Locate every parasitized RBC.
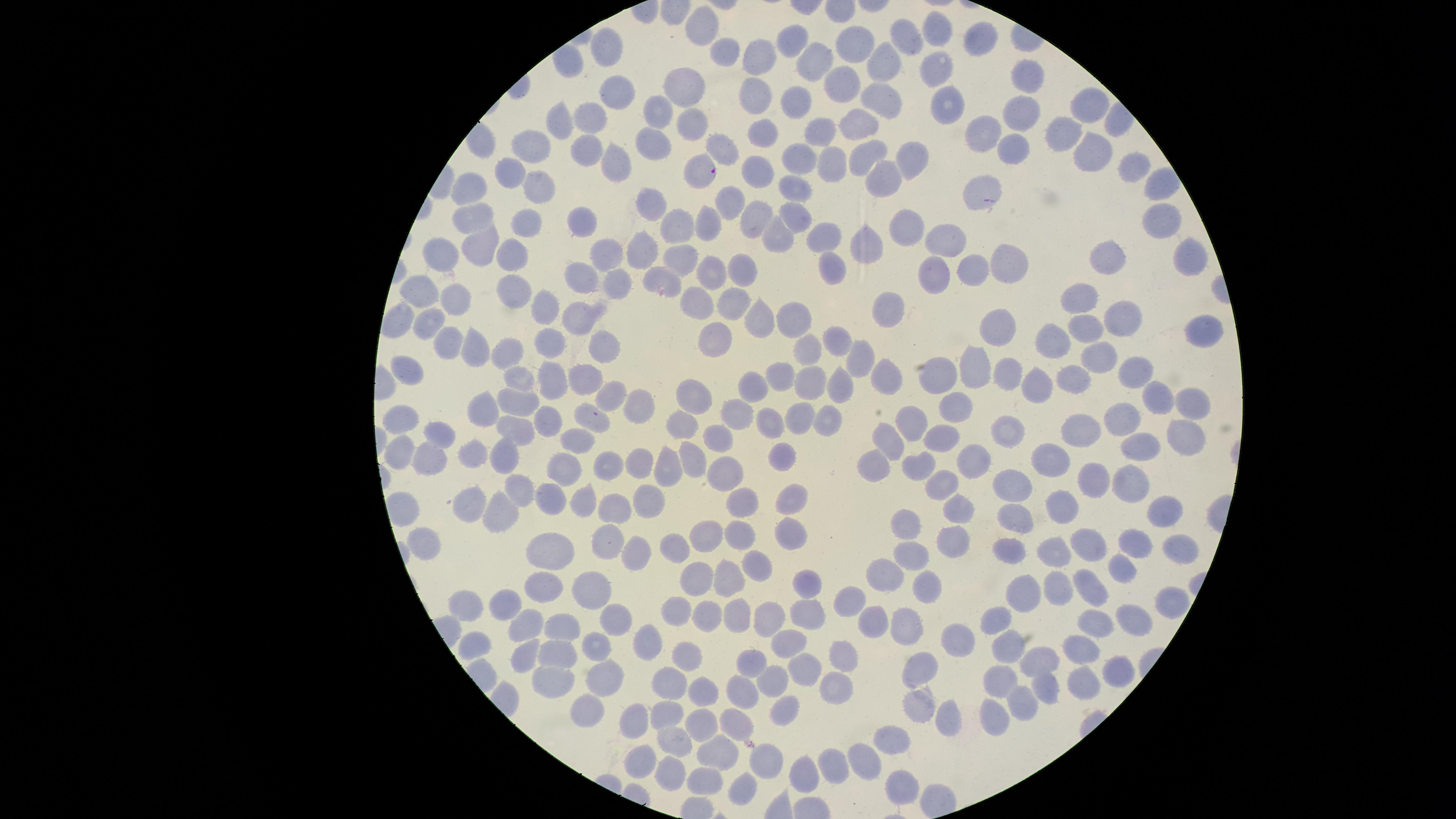

Approximate marker points, in pixels from the top-left corner.
Parasitized RBCs: (x=697, y=171).

visible region = circular
preparation = thin blood smear
image size = 1456×819 pixels
species = Plasmodium falciparum
stain = Giemsa
field of view = single
capture = smartphone photograph through the microscope eyepiece
uninfected RBCs = approximate marker points, in pixels from the top-left corner: (x=694, y=26), (x=935, y=28), (x=978, y=36), (x=792, y=39), (x=907, y=39), (x=855, y=41), (x=601, y=47), (x=726, y=53), (x=766, y=62), (x=812, y=62), (x=883, y=62), (x=933, y=64), (x=1027, y=79), (x=849, y=86), (x=677, y=90), (x=625, y=91), (x=882, y=95), (x=755, y=96), (x=949, y=102), (x=795, y=104), (x=1081, y=107), (x=1025, y=109), (x=657, y=115), (x=585, y=116), (x=563, y=119), (x=860, y=122), (x=693, y=125), (x=822, y=127), (x=764, y=130), (x=983, y=132), (x=1061, y=136), (x=535, y=142), (x=651, y=145), (x=1092, y=145), (x=725, y=147), (x=1008, y=147), (x=584, y=150), (x=867, y=154), (x=798, y=156), (x=913, y=158), (x=826, y=160), (x=617, y=164), (x=1131, y=168), (x=515, y=171), (x=754, y=172), (x=889, y=173), (x=982, y=185), (x=537, y=186), (x=793, y=186), (x=471, y=189), (x=726, y=205), (x=653, y=206), (x=797, y=213), (x=756, y=214), (x=474, y=216), (x=524, y=219), (x=1158, y=220), (x=586, y=222), (x=901, y=225), (x=675, y=227), (x=709, y=227), (x=777, y=236), (x=825, y=236), (x=947, y=238), (x=855, y=245), (x=484, y=248), (x=607, y=250), (x=643, y=250), (x=504, y=253), (x=443, y=254), (x=1103, y=255), (x=683, y=258), (x=1186, y=258), (x=1012, y=261), (x=738, y=265), (x=829, y=266), (x=973, y=267), (x=935, y=271), (x=582, y=272), (x=709, y=275), (x=666, y=276), (x=618, y=282), (x=510, y=287), (x=425, y=291), (x=1083, y=296), (x=457, y=297), (x=698, y=299), (x=732, y=302), (x=889, y=306), (x=542, y=307), (x=757, y=314), (x=1118, y=314), (x=795, y=316), (x=397, y=319), (x=578, y=322), (x=425, y=324), (x=992, y=325), (x=1086, y=328), (x=1201, y=328), (x=712, y=336), (x=1050, y=336), (x=550, y=337), (x=840, y=341), (x=448, y=342), (x=471, y=344), (x=603, y=345), (x=503, y=351), (x=1098, y=353), (x=813, y=357), (x=860, y=362), (x=973, y=362), (x=406, y=366), (x=1130, y=370), (x=1009, y=372), (x=778, y=376), (x=1072, y=376), (x=883, y=377), (x=517, y=378), (x=935, y=378), (x=584, y=382), (x=810, y=382), (x=839, y=382), (x=752, y=384), (x=1036, y=385), (x=691, y=394), (x=1159, y=395), (x=610, y=398), (x=638, y=402), (x=519, y=403), (x=1190, y=403), (x=953, y=405), (x=482, y=406), (x=738, y=408), (x=401, y=413), (x=547, y=417), (x=803, y=417), (x=912, y=417), (x=773, y=418), (x=825, y=419), (x=1125, y=420), (x=683, y=421), (x=588, y=423), (x=513, y=427), (x=439, y=429), (x=1087, y=431), (x=1186, y=432), (x=1003, y=436), (x=887, y=437), (x=941, y=438), (x=719, y=439), (x=572, y=440), (x=1138, y=440), (x=473, y=446), (x=402, y=453), (x=507, y=454), (x=784, y=454), (x=1056, y=456), (x=424, y=458), (x=969, y=459), (x=639, y=460), (x=695, y=460), (x=881, y=460), (x=921, y=462), (x=605, y=464), (x=666, y=469), (x=730, y=469), (x=559, y=472), (x=1132, y=480), (x=937, y=482), (x=1097, y=482), (x=1019, y=483), (x=521, y=491), (x=646, y=494), (x=544, y=496), (x=582, y=496), (x=793, y=497), (x=474, y=502), (x=747, y=502), (x=1059, y=503), (x=617, y=506), (x=958, y=506), (x=503, y=509), (x=1012, y=513), (x=1160, y=513), (x=902, y=523), (x=740, y=533), (x=797, y=534), (x=423, y=538), (x=953, y=538), (x=552, y=539), (x=609, y=541), (x=1081, y=541), (x=702, y=542), (x=1016, y=545), (x=1130, y=545), (x=1177, y=546), (x=1052, y=550), (x=639, y=551), (x=677, y=553), (x=913, y=554), (x=756, y=562), (x=1121, y=565), (x=885, y=569), (x=730, y=575), (x=806, y=582), (x=541, y=583), (x=693, y=583), (x=925, y=583), (x=1059, y=586), (x=595, y=589), (x=1087, y=589), (x=1025, y=590), (x=511, y=598), (x=849, y=601), (x=1168, y=602), (x=465, y=605), (x=678, y=606), (x=807, y=608), (x=705, y=610), (x=736, y=611), (x=620, y=614), (x=766, y=615), (x=997, y=615), (x=1133, y=616), (x=873, y=620), (x=525, y=623), (x=909, y=624), (x=1094, y=624), (x=565, y=625), (x=963, y=631), (x=647, y=638), (x=793, y=641), (x=592, y=642), (x=1011, y=642), (x=473, y=644), (x=1085, y=645), (x=523, y=655), (x=564, y=655), (x=683, y=656), (x=841, y=658), (x=752, y=660), (x=1045, y=660), (x=803, y=667), (x=922, y=667), (x=1114, y=670), (x=607, y=675), (x=996, y=678), (x=561, y=679), (x=775, y=680), (x=1080, y=680), (x=672, y=682), (x=1049, y=684), (x=839, y=685), (x=742, y=690), (x=703, y=693), (x=1025, y=698), (x=789, y=710), (x=915, y=710), (x=662, y=715), (x=999, y=715), (x=584, y=717), (x=705, y=718), (x=954, y=718), (x=733, y=719), (x=632, y=720), (x=678, y=739), (x=897, y=739), (x=718, y=746), (x=640, y=763), (x=867, y=763), (x=773, y=766), (x=832, y=767), (x=803, y=773), (x=671, y=775), (x=703, y=778), (x=742, y=785), (x=908, y=786)